Report the malaria status of this cell.
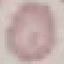

It is uninfected.

capture = smartphone camera at the microscope eyepiece
stain = Giemsa
image type = automatically extracted cell patch, resized to 64 × 64 pixels
preparation = thin blood smear